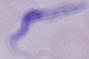

Summary:
  - Magnification: 1000x
  - Modality: photomicrograph
  - Identification: trypanosome